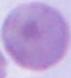
Summary:
  - Modality: photomicrograph
  - Identification: red blood cell
  - Magnification: 1000x